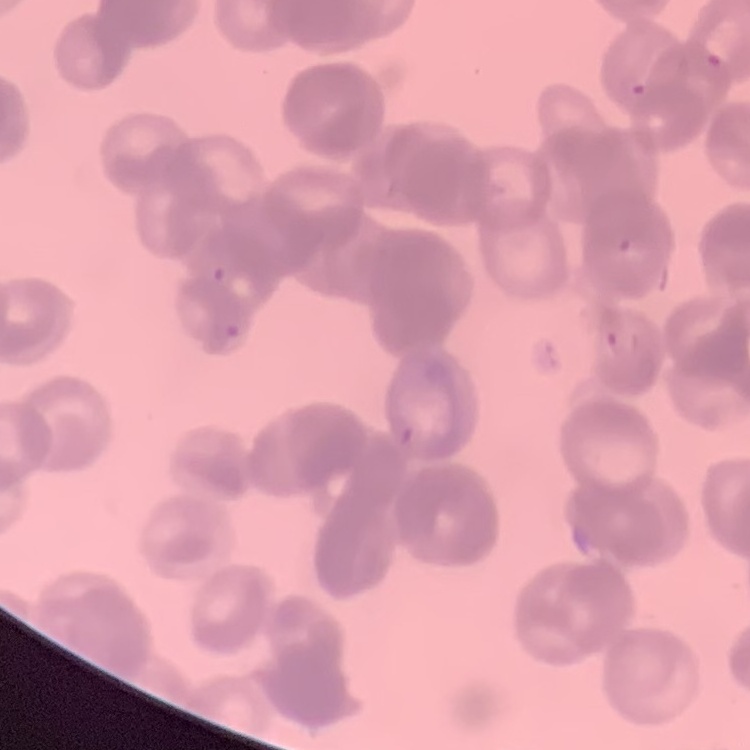

Summary:
  - Red blood cell morphology: rouleaux formation
  - Image type: one tile cut from a larger photomicrograph
  - Preparation: thin blood film
  - Stain: Field's or Giemsa